Locate every Plasmodium parasite.
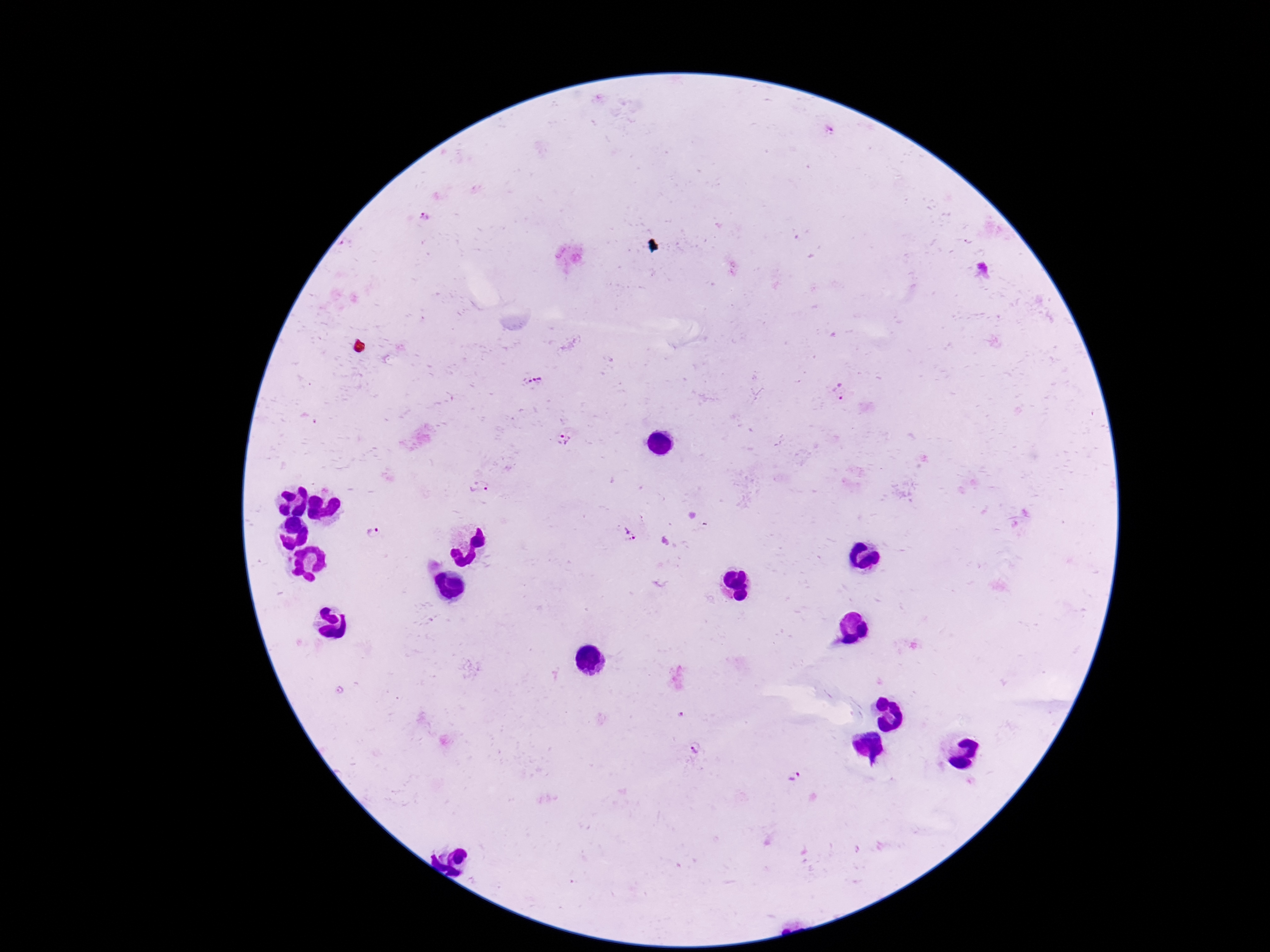
Approximate centers as (x, y) in pixels.
Plasmodium parasites: (536, 380), (842, 393), (563, 438), (478, 487), (372, 535), (629, 536), (696, 751), (794, 776).

{
  "stain": "Giemsa",
  "magnification": "100x",
  "capture": "smartphone camera through the microscope eyepiece",
  "preparation": "thick peripheral-blood smear",
  "field_of_view": "single",
  "patient_malaria_status": "positive",
  "image_size": "1270×952 pixels"
}